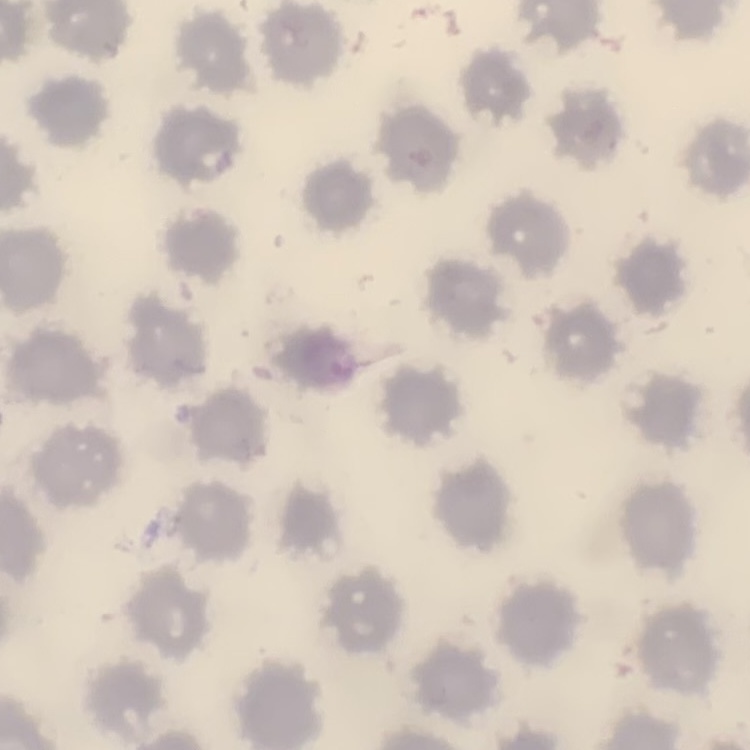
The erythrocytes show no rouleaux formation. Stained with either Field's or Giemsa. Thin peripheral smear. One tile cut from a larger photomicrograph.